Assess the morphology of the red blood cells.
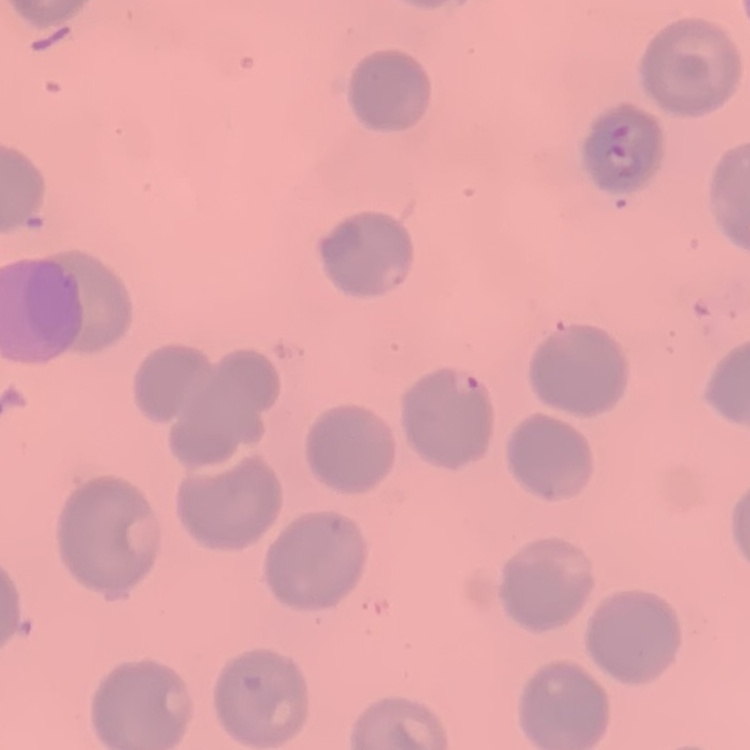

No rouleaux formation.

Summary:
  - Image type: one tile cut from a larger photomicrograph
  - Stain: Field's or Giemsa
  - Preparation: thin blood film